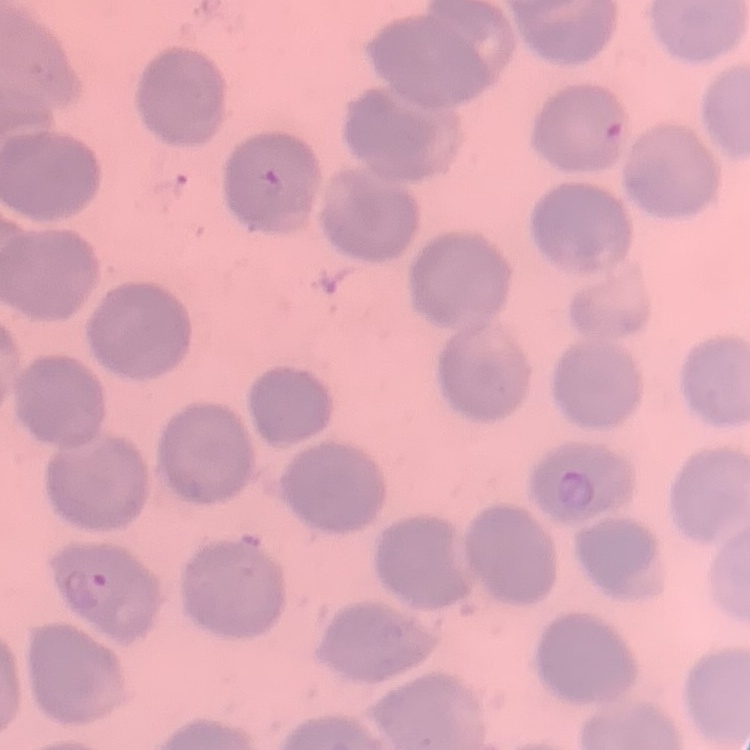 The erythrocytes exhibit no rouleaux formation. One tile cut from a larger photomicrograph. Field's or Giemsa stain. Thin blood smear.